Report the malaria status of this cell.
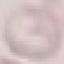
It is uninfected.

{
  "preparation": "thin smear",
  "stain": "Giemsa",
  "capture": "smartphone camera at the microscope eyepiece",
  "image_type": "automatically extracted cell patch, resized to 64 × 64 pixels"
}